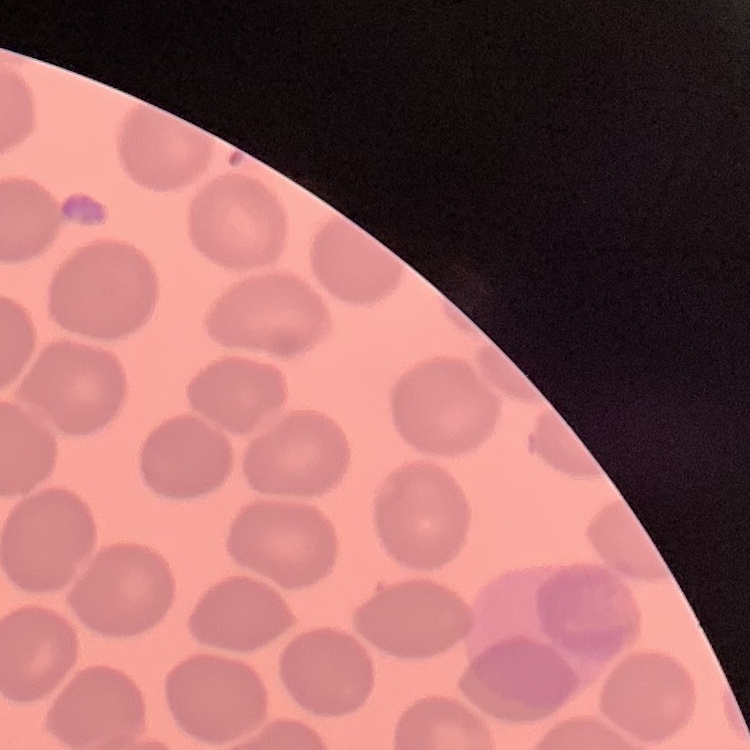
The erythrocytes show no rouleaux formation. Field's or Giemsa stain. Thin blood film. One tile cut from a larger photomicrograph.